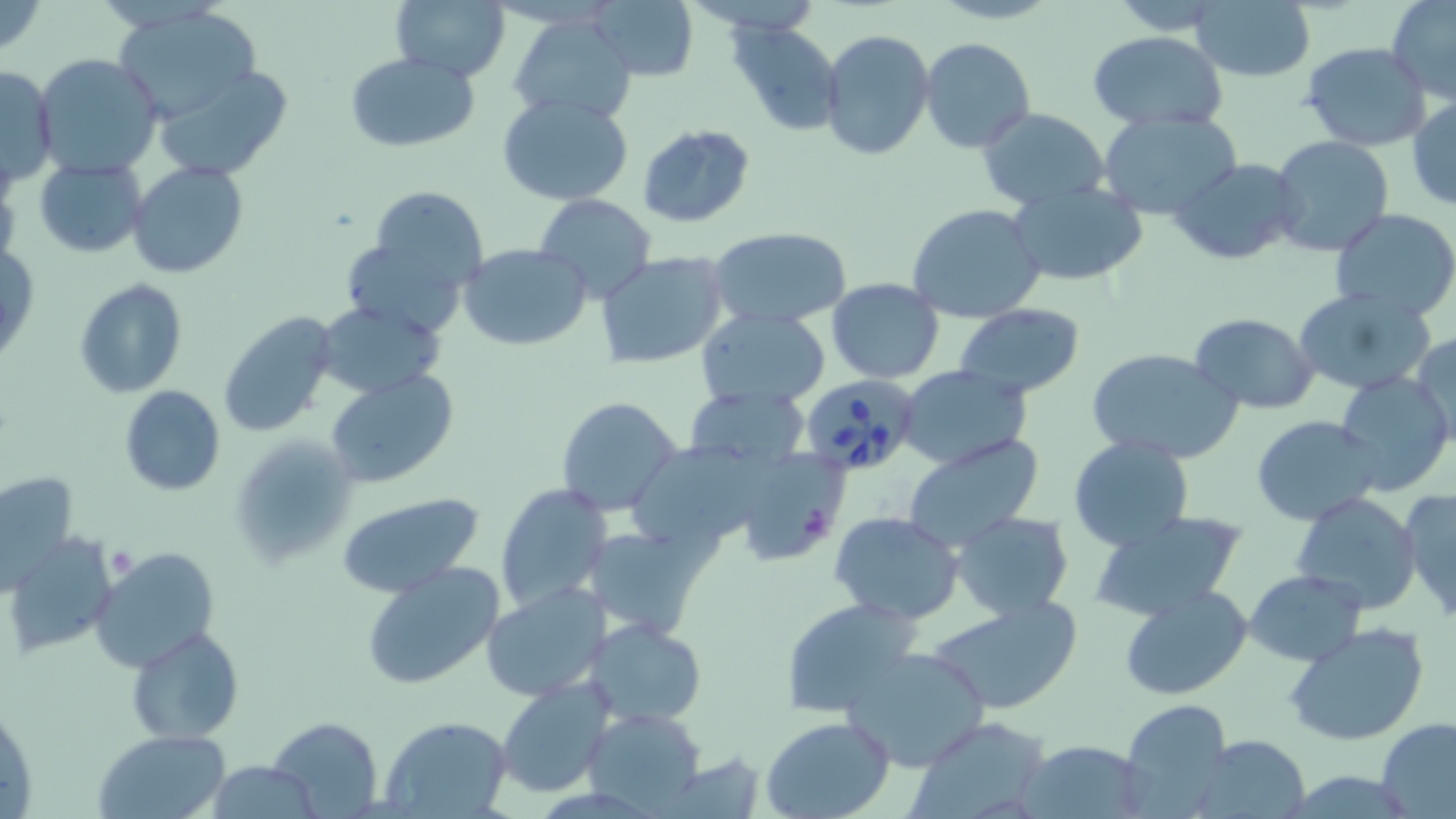
slide-level diagnosis = Babesia divergens
image size = 1456×819 pixels
preparation = thin blood film
uninfected red blood cell locations = approximate bounding boxes as [x1, y1, x2, y2] in pixels: [0, 0, 46, 54], [588, 0, 699, 82], [1388, 0, 1456, 104], [391, 1, 510, 80], [1191, 2, 1316, 83], [114, 5, 265, 118], [509, 12, 638, 123], [730, 24, 843, 135], [818, 29, 935, 160], [1085, 31, 1228, 130], [920, 36, 1034, 153], [1301, 42, 1431, 151], [345, 52, 479, 151], [34, 54, 161, 179], [153, 65, 292, 181], [1, 66, 59, 189], [499, 93, 634, 204], [1408, 97, 1456, 213], [977, 108, 1109, 208], [1097, 109, 1242, 219], [637, 125, 757, 229], [1269, 135, 1393, 256], [34, 158, 149, 258], [1169, 158, 1302, 267], [128, 162, 249, 277], [1006, 182, 1149, 286], [364, 184, 487, 289], [532, 194, 657, 302], [905, 202, 1046, 323], [1330, 208, 1456, 318], [472, 217, 652, 329], [709, 227, 852, 329], [341, 234, 473, 335], [1, 240, 40, 365], [459, 242, 591, 350], [595, 250, 731, 370], [827, 277, 945, 383], [75, 279, 188, 398], [1292, 286, 1437, 397], [316, 300, 446, 399], [954, 303, 1087, 399], [695, 307, 831, 411], [218, 311, 339, 437], [1189, 312, 1318, 414], [1409, 331, 1456, 446], [1086, 346, 1243, 464], [898, 366, 1031, 471], [326, 370, 458, 486], [1335, 372, 1453, 494], [118, 385, 225, 496], [683, 387, 812, 472], [556, 396, 686, 519], [1252, 415, 1387, 524], [903, 434, 1042, 548], [1067, 436, 1195, 554], [237, 442, 358, 563], [633, 444, 771, 554], [721, 445, 851, 566], [2, 469, 77, 584], [495, 482, 613, 611], [1398, 487, 1456, 625], [336, 490, 485, 600], [1289, 491, 1424, 613], [1089, 509, 1251, 622], [829, 510, 965, 624], [951, 511, 1074, 618], [582, 526, 704, 636], [7, 536, 118, 654], [91, 546, 220, 674], [361, 562, 503, 691], [1246, 569, 1365, 666], [482, 582, 611, 701], [1119, 584, 1253, 702], [780, 595, 924, 717], [926, 597, 1083, 715], [586, 618, 708, 726], [1282, 621, 1432, 749], [126, 625, 243, 744], [840, 645, 994, 771], [498, 678, 616, 798], [1121, 700, 1232, 811], [583, 706, 706, 812], [378, 714, 513, 817], [265, 716, 382, 818], [761, 716, 895, 819], [903, 716, 1053, 819], [1377, 718, 1456, 818], [96, 729, 230, 817], [1193, 734, 1311, 819], [1018, 738, 1148, 817], [207, 760, 323, 817]
magnification = 1000x
Babesia divergens-infected red blood cell locations = approximate bounding boxes as [x1, y1, x2, y2] in pixels: [802, 376, 921, 474]
modality = optical microscopy
stain = May-Grünwald-Giemsa
field of view = single
platelet locations = approximate bounding boxes as [x1, y1, x2, y2] in pixels: [107, 546, 137, 582]